Outline every Plasmodium parasite, every leukocyte, and every artifact (stain precipitate or debris).
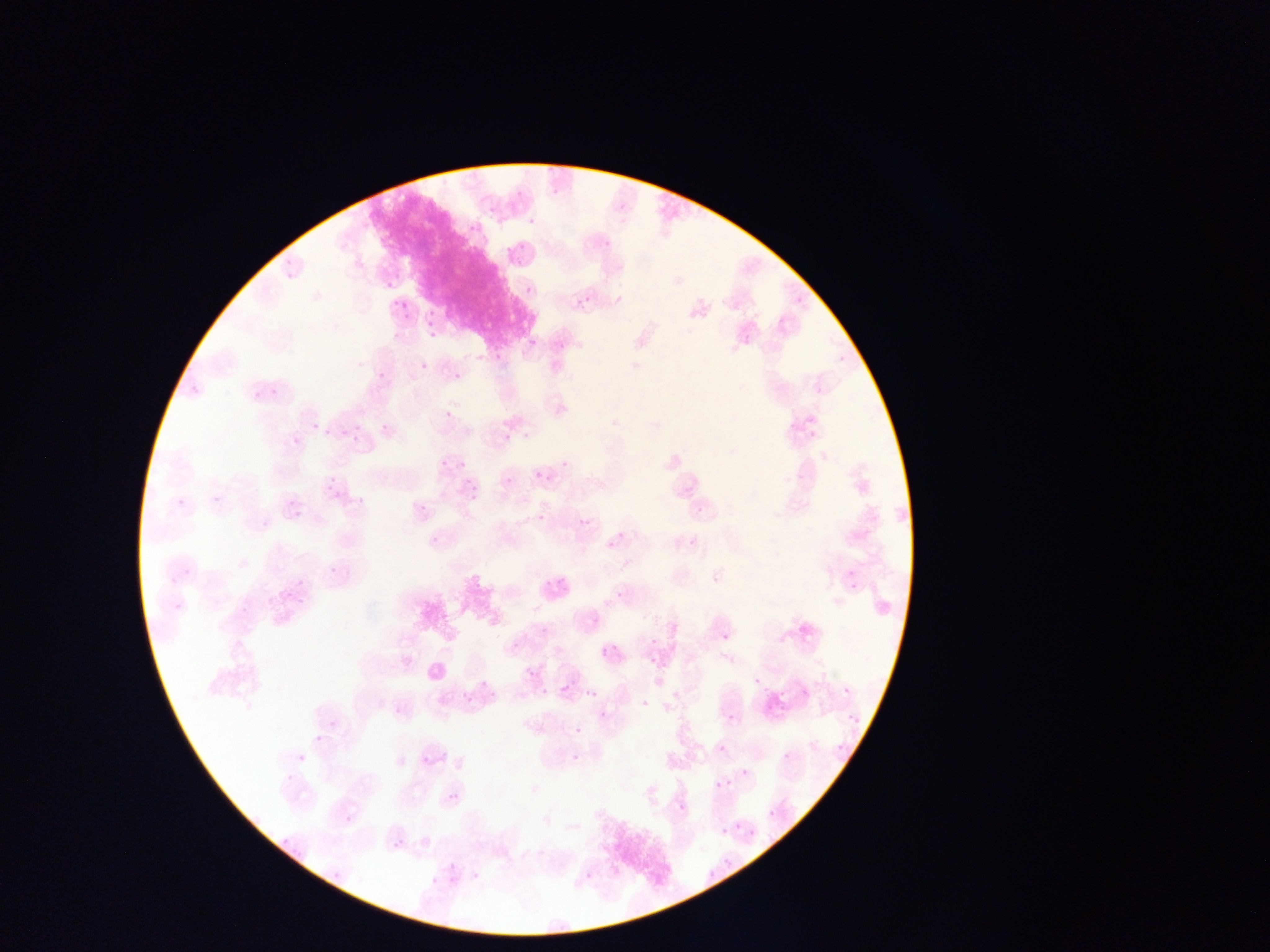
Approximate bounding boxes as (left, top, right, bottom) in pixels.
Plasmodium parasites: (521, 212, 534, 229), (460, 214, 480, 235), (501, 242, 513, 256), (282, 249, 296, 268), (282, 267, 295, 281), (525, 285, 534, 295), (395, 298, 413, 316), (575, 298, 586, 309), (425, 308, 438, 328), (429, 338, 440, 343), (529, 339, 537, 347), (553, 339, 565, 350), (420, 362, 429, 372), (376, 370, 388, 382), (453, 372, 462, 382), (269, 380, 284, 401), (249, 383, 262, 398), (445, 411, 454, 421), (310, 415, 319, 428), (372, 418, 388, 429), (324, 427, 330, 439), (342, 430, 349, 438), (350, 431, 359, 443), (522, 432, 531, 440), (502, 433, 511, 443), (292, 436, 301, 445), (558, 450, 574, 470), (436, 454, 447, 469), (455, 454, 475, 476), (535, 471, 544, 480), (505, 478, 513, 487), (327, 481, 337, 491), (465, 491, 476, 508), (212, 494, 223, 504), (176, 497, 188, 509), (417, 500, 424, 511), (696, 506, 703, 514), (573, 510, 588, 523), (293, 511, 302, 520), (538, 514, 545, 522), (614, 526, 628, 550), (429, 533, 444, 549), (598, 533, 614, 548), (689, 537, 699, 547), (326, 561, 343, 578), (846, 567, 860, 582), (178, 568, 196, 575), (163, 570, 179, 588), (535, 572, 553, 592), (298, 573, 308, 590), (560, 577, 573, 590), (281, 581, 294, 602), (611, 588, 624, 602), (170, 595, 190, 616), (536, 624, 549, 637), (722, 633, 731, 642), (650, 636, 659, 646), (512, 644, 520, 653), (601, 647, 610, 657), (527, 668, 537, 679), (556, 677, 567, 692), (479, 680, 489, 690), (582, 680, 599, 700), (536, 686, 550, 697), (843, 686, 852, 695), (463, 693, 474, 704), (598, 710, 608, 721), (727, 713, 735, 722), (328, 719, 338, 730), (575, 727, 583, 735), (315, 736, 323, 744), (835, 743, 847, 755), (718, 744, 726, 753), (783, 753, 791, 761), (572, 755, 581, 764), (741, 768, 749, 777), (716, 781, 724, 789), (449, 793, 460, 804), (677, 801, 686, 810), (768, 811, 775, 819), (344, 814, 354, 824), (734, 823, 741, 831), (721, 827, 731, 835), (385, 832, 403, 854), (447, 864, 455, 873), (471, 871, 481, 881), (429, 876, 440, 888) | approximate (x, y) pixel centers of objects too small to bound: (477, 356), (497, 357), (758, 680), (645, 704), (301, 759).
No leukocytes observed.

country = Ghana
capture = mobile-phone photograph through a microscope
preparation = thin blood film
image size = 1270×952 pixels
field of view = single